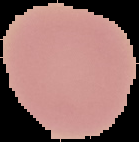

image type = segmented cell region with the area outside set to black
image size = 139×142 pixels
preparation = thin blood film
malaria status = uninfected